Assess the morphology of the erythrocytes.
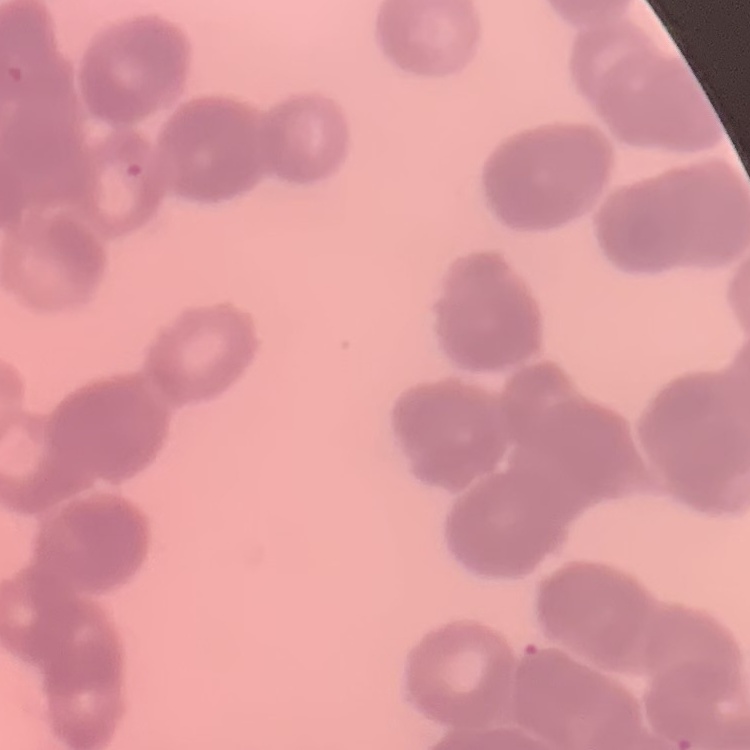
Rouleaux formation.

{
  "stain": "Field's or Giemsa",
  "preparation": "thin blood film",
  "image_type": "square crop of a larger photomicrograph"
}